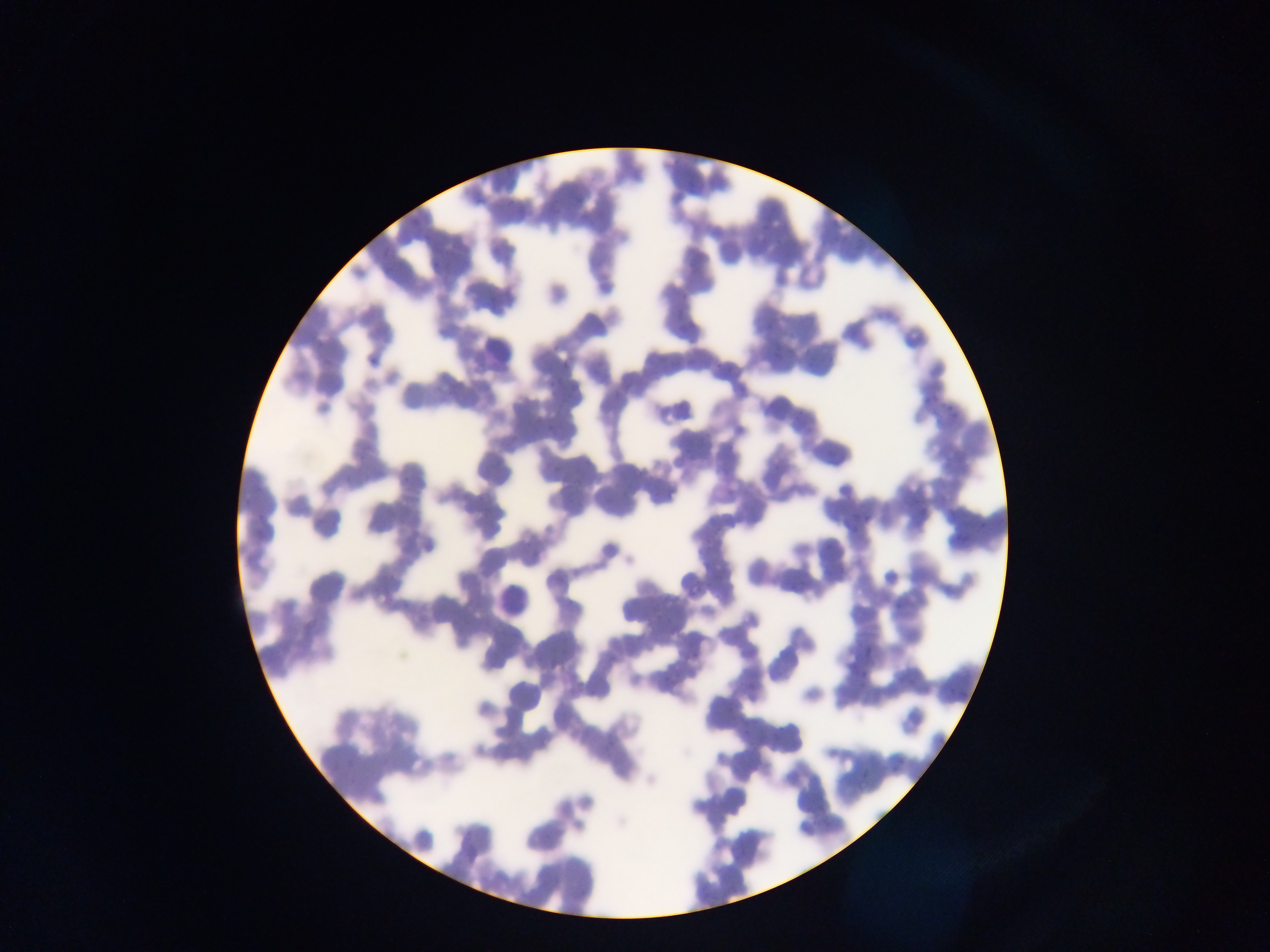

leukocyte locations = approximate bounding boxes as left top right bottom in pixels: 480 327 518 363; 491 560 536 618
image size = 1270×952 pixels
field of view = single
malaria parasite locations = approximate bounding boxes as left top right bottom in pixels: 560 352 571 369
capture = mobile-phone photograph through a microscope
country = Ghana
preparation = thin blood smear